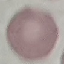 Malaria status: uninfected. Thin blood smear. Automatically extracted cell patch, resized to 64 × 64 pixels. Acquired by smartphone through the microscope eyepiece. Giemsa stain.